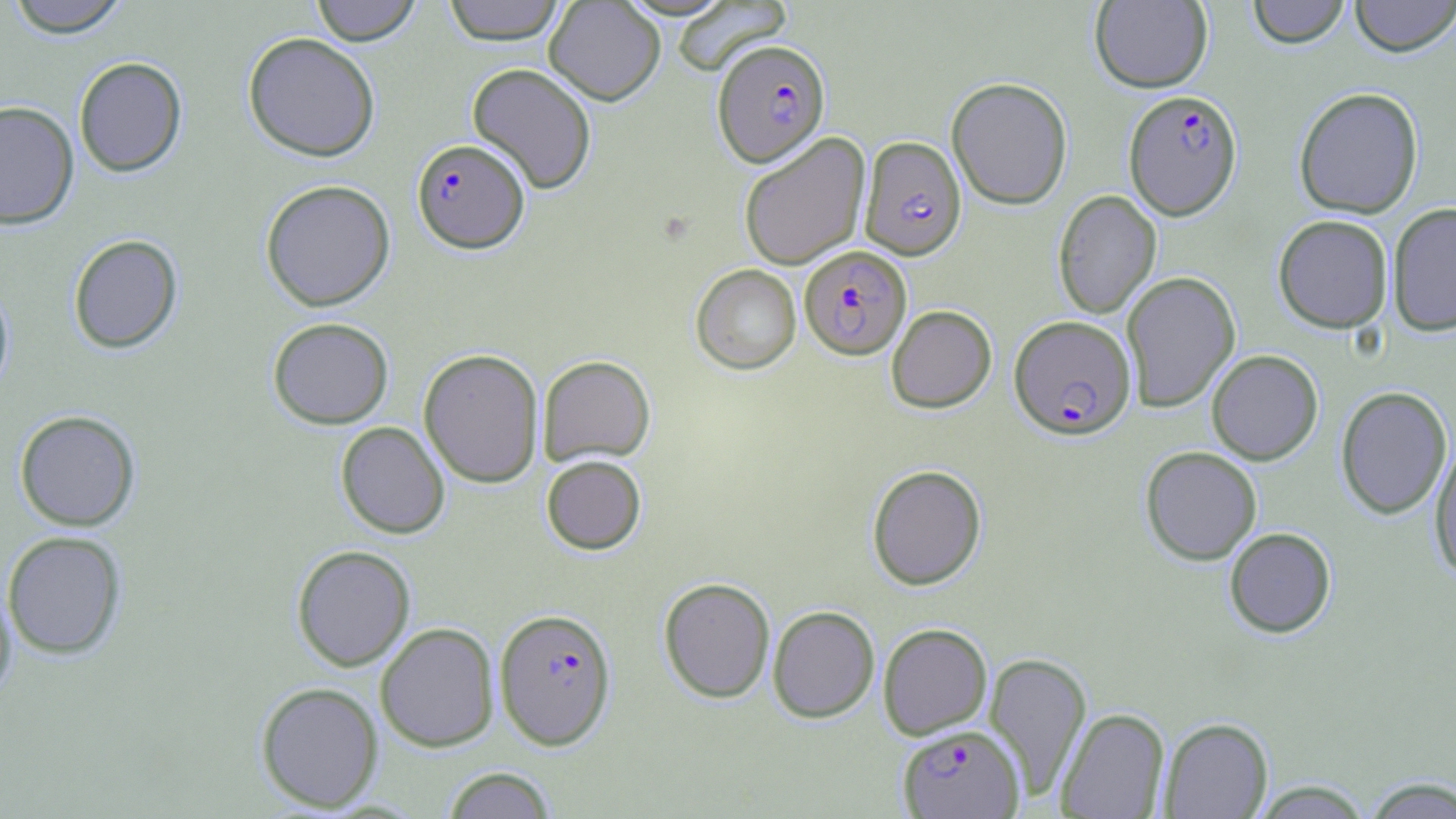
Summary:
  - Coordinate format: approximate bounding boxes as [x1, y1, x2, y2] in pixels
  - Uninfected red blood cell locations: [4, 0, 132, 38], [310, 0, 421, 45], [442, 0, 566, 44], [544, 0, 666, 105], [1090, 0, 1213, 93], [1246, 0, 1351, 48], [1349, 0, 1456, 57], [671, 1, 792, 76], [242, 32, 380, 161], [74, 56, 187, 177], [466, 62, 598, 194], [946, 77, 1073, 209], [1293, 86, 1424, 219], [0, 101, 79, 229], [738, 132, 870, 270], [260, 179, 395, 311], [1053, 190, 1161, 319], [1387, 202, 1456, 337], [1273, 214, 1393, 333], [67, 233, 183, 353], [690, 264, 801, 375], [1120, 271, 1240, 412], [0, 277, 15, 400], [886, 305, 996, 413], [267, 316, 394, 429], [418, 347, 544, 487], [1206, 349, 1323, 465], [537, 354, 656, 466], [1335, 386, 1452, 519], [14, 409, 141, 531], [335, 421, 450, 539], [1429, 437, 1456, 581], [1140, 445, 1262, 565], [541, 455, 646, 554], [866, 464, 986, 590], [1224, 527, 1336, 638], [2, 530, 127, 659], [291, 545, 416, 671], [658, 577, 776, 704], [0, 578, 17, 703], [658, 596, 881, 712], [767, 605, 880, 723], [375, 622, 499, 752], [877, 623, 992, 740], [984, 651, 1092, 801], [254, 681, 384, 812], [1056, 708, 1170, 818], [1159, 717, 1273, 818], [441, 766, 557, 818], [1360, 776, 1456, 818], [1249, 780, 1375, 818]
  - Plasmodium falciparum-infected red blood cell locations: [713, 39, 830, 167], [1123, 90, 1241, 218], [859, 136, 966, 260], [412, 138, 529, 253], [799, 245, 912, 360], [1009, 314, 1136, 439], [494, 607, 617, 750], [897, 724, 1024, 818]
  - Slide-level diagnosis: Plasmodium falciparum
  - Stain: May-Grünwald-Giemsa
  - Image size: 1456×819 pixels
  - Preparation: thin blood smear
  - Magnification: 1000x
  - Field of view: single
  - Modality: optical microscopy